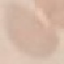
result: negative for malaria parasites
preparation: thin blood smear
stain: Giemsa
image_type: cell patch, automatically extracted from a larger field of view and resized to 64 × 64 pixels
capture: smartphone camera at the microscope eyepiece